Outline each blood parasite and name the species.
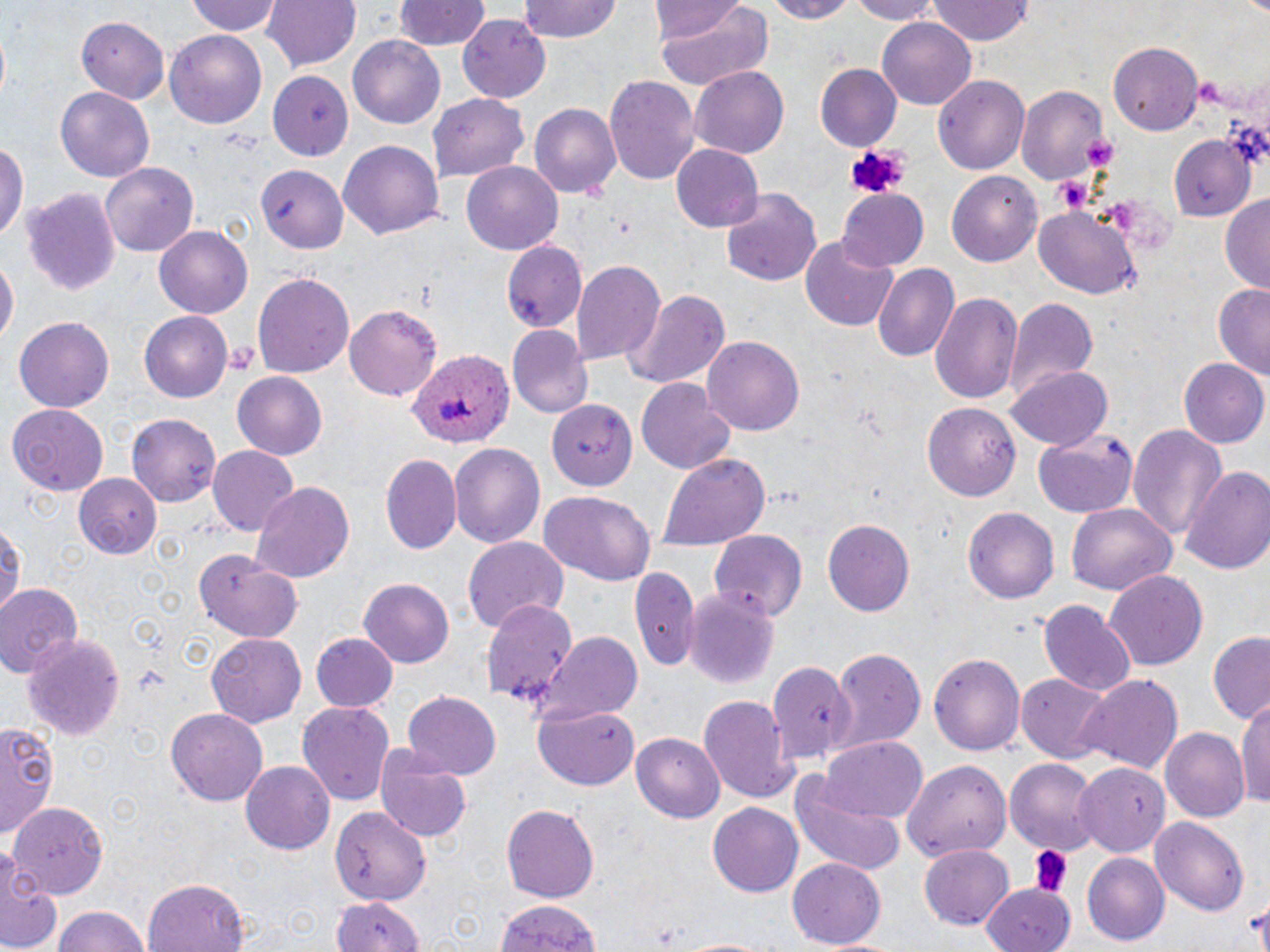
Approximate bounding boxes as named x1/y1/x2/y2 corners in pixels.
Plasmodium ovale-infected red blood cells: (x1=404, y1=350, x2=514, y2=448).
No Plasmodium falciparum, Plasmodium malariae, Plasmodium vivax, Babesia divergens, or Trypanosoma brucei observed.

slide-level diagnosis = Plasmodium ovale
magnification = 1000x
field of view = one of a larger specimen
uninfected red blood cell locations = approximate bounding boxes as named x1/y1/x2/y2 corners in pixels: (x1=184, y1=0, x2=283, y2=37), (x1=262, y1=0, x2=360, y2=73), (x1=393, y1=0, x2=487, y2=51), (x1=516, y1=0, x2=623, y2=43), (x1=652, y1=0, x2=753, y2=47), (x1=652, y1=0, x2=772, y2=88), (x1=762, y1=0, x2=855, y2=22), (x1=844, y1=0, x2=946, y2=23), (x1=927, y1=0, x2=1036, y2=46), (x1=456, y1=14, x2=552, y2=101), (x1=877, y1=14, x2=977, y2=107), (x1=75, y1=15, x2=169, y2=103), (x1=165, y1=30, x2=266, y2=126), (x1=348, y1=37, x2=443, y2=127), (x1=1109, y1=41, x2=1202, y2=135), (x1=815, y1=64, x2=900, y2=148), (x1=690, y1=65, x2=788, y2=156), (x1=270, y1=70, x2=354, y2=160), (x1=605, y1=74, x2=700, y2=184), (x1=932, y1=74, x2=1031, y2=175), (x1=1017, y1=83, x2=1110, y2=186), (x1=56, y1=86, x2=153, y2=183), (x1=429, y1=94, x2=532, y2=182), (x1=528, y1=103, x2=620, y2=199), (x1=1167, y1=136, x2=1253, y2=223), (x1=338, y1=140, x2=445, y2=239), (x1=0, y1=141, x2=26, y2=247), (x1=670, y1=144, x2=765, y2=232), (x1=461, y1=162, x2=563, y2=254), (x1=100, y1=163, x2=200, y2=257), (x1=256, y1=167, x2=347, y2=255), (x1=946, y1=170, x2=1041, y2=265), (x1=21, y1=187, x2=121, y2=296), (x1=721, y1=190, x2=822, y2=286), (x1=836, y1=190, x2=930, y2=272), (x1=1218, y1=195, x2=1270, y2=293), (x1=1033, y1=205, x2=1141, y2=300), (x1=154, y1=227, x2=251, y2=317), (x1=798, y1=236, x2=900, y2=332), (x1=501, y1=240, x2=589, y2=331), (x1=0, y1=255, x2=17, y2=345), (x1=574, y1=261, x2=665, y2=364), (x1=871, y1=264, x2=958, y2=363), (x1=254, y1=270, x2=354, y2=378), (x1=1212, y1=283, x2=1270, y2=383), (x1=622, y1=287, x2=728, y2=391), (x1=931, y1=292, x2=1022, y2=406), (x1=1004, y1=297, x2=1098, y2=398), (x1=345, y1=303, x2=441, y2=401), (x1=139, y1=312, x2=234, y2=401), (x1=12, y1=316, x2=115, y2=412), (x1=507, y1=327, x2=591, y2=417), (x1=704, y1=335, x2=804, y2=434), (x1=1181, y1=357, x2=1269, y2=450), (x1=1009, y1=365, x2=1113, y2=450), (x1=232, y1=372, x2=328, y2=460), (x1=637, y1=380, x2=736, y2=474), (x1=550, y1=400, x2=638, y2=488), (x1=924, y1=402, x2=1021, y2=500), (x1=7, y1=404, x2=108, y2=495), (x1=127, y1=417, x2=220, y2=505), (x1=1129, y1=422, x2=1229, y2=546), (x1=1032, y1=429, x2=1139, y2=516), (x1=448, y1=443, x2=545, y2=548), (x1=207, y1=446, x2=298, y2=536), (x1=656, y1=452, x2=771, y2=551), (x1=381, y1=456, x2=461, y2=555), (x1=1184, y1=465, x2=1270, y2=577), (x1=72, y1=474, x2=164, y2=558), (x1=251, y1=482, x2=356, y2=584), (x1=538, y1=490, x2=656, y2=585), (x1=1067, y1=505, x2=1176, y2=597), (x1=962, y1=507, x2=1058, y2=604), (x1=822, y1=518, x2=915, y2=616), (x1=0, y1=519, x2=24, y2=619), (x1=709, y1=527, x2=809, y2=620), (x1=462, y1=536, x2=567, y2=633), (x1=193, y1=550, x2=301, y2=642), (x1=632, y1=566, x2=699, y2=665), (x1=1105, y1=570, x2=1208, y2=670), (x1=357, y1=578, x2=453, y2=670), (x1=0, y1=582, x2=84, y2=681), (x1=683, y1=588, x2=780, y2=688), (x1=482, y1=600, x2=578, y2=708), (x1=1040, y1=600, x2=1136, y2=697), (x1=205, y1=632, x2=307, y2=726), (x1=1206, y1=632, x2=1270, y2=724), (x1=24, y1=633, x2=124, y2=741), (x1=311, y1=633, x2=399, y2=710), (x1=535, y1=633, x2=643, y2=722), (x1=827, y1=648, x2=926, y2=751), (x1=929, y1=650, x2=1026, y2=754), (x1=770, y1=659, x2=856, y2=763), (x1=1072, y1=672, x2=1183, y2=776), (x1=1016, y1=675, x2=1112, y2=763), (x1=402, y1=690, x2=501, y2=778), (x1=1238, y1=692, x2=1270, y2=814), (x1=699, y1=695, x2=799, y2=801), (x1=296, y1=702, x2=395, y2=808), (x1=165, y1=706, x2=269, y2=805), (x1=534, y1=706, x2=639, y2=790), (x1=0, y1=722, x2=60, y2=836), (x1=1162, y1=728, x2=1249, y2=823), (x1=631, y1=730, x2=724, y2=819), (x1=820, y1=738, x2=927, y2=821), (x1=374, y1=745, x2=473, y2=843), (x1=1005, y1=759, x2=1098, y2=851), (x1=240, y1=760, x2=335, y2=853), (x1=903, y1=762, x2=1012, y2=861), (x1=1074, y1=762, x2=1167, y2=855), (x1=788, y1=774, x2=907, y2=879), (x1=12, y1=800, x2=110, y2=898), (x1=708, y1=801, x2=803, y2=897), (x1=502, y1=802, x2=597, y2=905), (x1=327, y1=804, x2=431, y2=906), (x1=1151, y1=816, x2=1250, y2=917), (x1=918, y1=843, x2=1014, y2=929), (x1=1082, y1=853, x2=1169, y2=945), (x1=0, y1=854, x2=61, y2=951), (x1=787, y1=858, x2=884, y2=949), (x1=144, y1=876, x2=251, y2=952), (x1=983, y1=884, x2=1069, y2=952), (x1=326, y1=894, x2=429, y2=952), (x1=492, y1=898, x2=604, y2=952), (x1=49, y1=904, x2=154, y2=952), (x1=673, y1=935, x2=780, y2=952)
stain = May-Grünwald-Giemsa
image size = 1270×952 pixels
platelet locations = approximate bounding boxes as named x1/y1/x2/y2 corners in pixels: (x1=1197, y1=79, x2=1226, y2=109), (x1=842, y1=143, x2=910, y2=200), (x1=1050, y1=175, x2=1090, y2=214), (x1=225, y1=342, x2=258, y2=379), (x1=1029, y1=844, x2=1072, y2=896)
modality = optical microscopy
preparation = thin blood smear